Assess this cell for malaria.
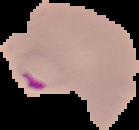
It is parasitized.

Image is 139×130 pixels. From a thin blood smear. Cell region segmented out of the field of view; the surrounding area is masked to black.